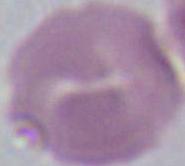
magnification = 1000x
modality = micrograph
identification = red blood cell